Classify this cell by malaria status.
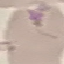

It is uninfected.

preparation = thin blood smear
image type = cell patch, automatically extracted from a larger field of view and resized to 64 × 64 pixels
capture = smartphone through the microscope eyepiece
stain = Giemsa